Locate leukocytes (white blood cells).
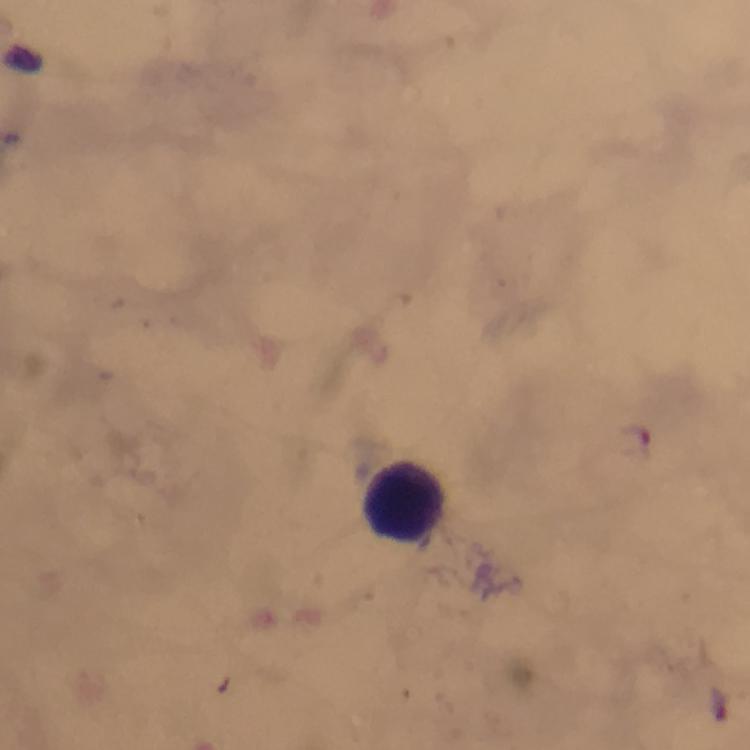

Approximate centers as [x, y] in pixels.
Leukocytes: [397, 495].

immersion oil = used
magnification = 100x
capture = smartphone photograph through a microscope
stain = Giemsa
image size = 750×750 pixels
preparation = thick blood smear
cropped from = a single field of view
Plasmodium parasites = none seen
context = from a malaria diagnostic workup